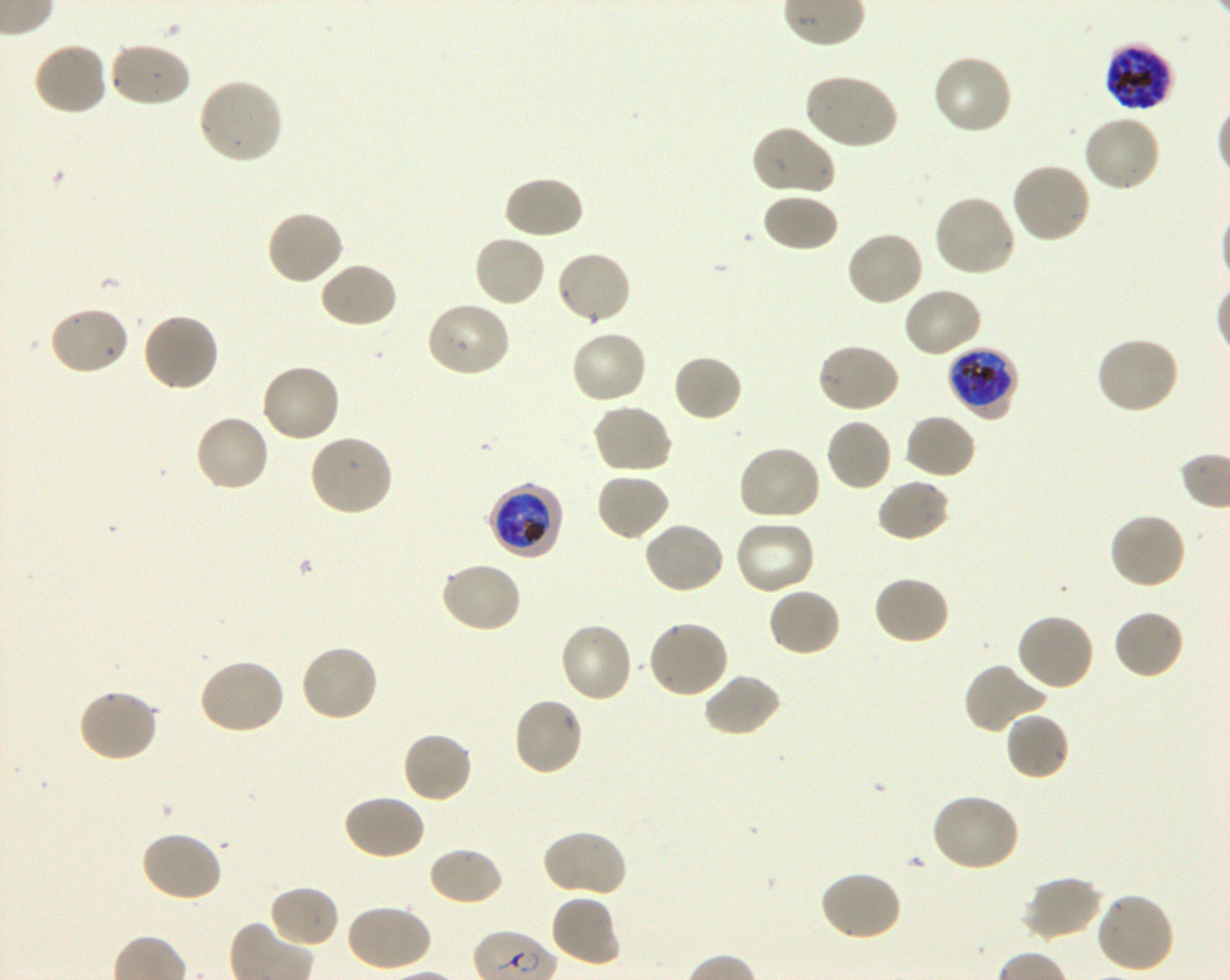

Not every red blood cell is marked. A life-cycle stage — or a range of stages, where the recorded stages span more than one — follows each staged infected red blood cell.
image_size: 1230×980 pixels
preparation: thin blood smear
culture: in-vitro P. falciparum strain 3D7, shaking
locations_of_infected_red_blood_cells: 'approximate bounding boxes as [x1, y1, x2, y2] in pixels: [1104, 43, 1171, 115] schizont; [949, 345, 1017, 423] late trophozoite to late schizont; [489, 483, 564, 560] early trophozoite to early schizont'
locations_of_uninfected_red_blood_cells: 'approximate bounding boxes as [x1, y1, x2, y2] in pixels: [32, 41, 109, 118], [108, 41, 192, 109], [932, 53, 1015, 136], [803, 73, 898, 151], [196, 77, 284, 165], [1082, 113, 1163, 193], [750, 124, 836, 197], [1011, 161, 1092, 244], [501, 174, 585, 241], [760, 192, 839, 253], [932, 194, 1016, 279], [266, 210, 344, 286], [845, 230, 925, 307], [473, 233, 546, 308], [554, 250, 632, 326], [318, 262, 397, 329], [902, 286, 983, 358], [425, 300, 512, 377], [47, 304, 131, 376], [141, 312, 221, 393], [569, 329, 649, 406], [1095, 336, 1181, 415], [815, 342, 901, 414], [672, 353, 744, 422], [259, 363, 341, 444], [591, 402, 674, 474], [904, 412, 977, 480], [193, 414, 270, 494], [825, 417, 893, 492], [308, 433, 395, 516], [735, 444, 821, 522], [594, 471, 670, 542], [876, 478, 951, 544], [1108, 512, 1188, 591], [734, 519, 816, 596], [642, 520, 725, 595], [439, 561, 522, 634], [872, 574, 951, 647], [767, 587, 842, 657], [1112, 608, 1185, 680], [1014, 612, 1095, 692], [646, 620, 730, 700], [558, 621, 634, 704], [299, 643, 379, 723], [197, 659, 286, 736], [962, 662, 1047, 735], [702, 672, 782, 738], [77, 689, 160, 764], [511, 696, 584, 777], [1003, 711, 1070, 782], [401, 731, 473, 804], [930, 793, 1020, 873], [343, 794, 426, 861], [540, 828, 628, 900], [139, 831, 223, 903], [427, 846, 504, 907], [818, 870, 903, 942], [1021, 874, 1102, 942], [269, 883, 341, 948], [1094, 891, 1175, 975], [550, 894, 621, 967], [345, 903, 432, 973]'
stain: Giemsa
objective: 100x, oil immersion, numerical aperture 1.30
donor_blood_group: O+
field_of_view: one from this slide